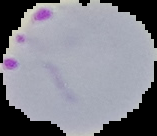

Image is 157×136 pixels. From a thin blood smear. Segmented cell region on a black background. Result: malaria parasites detected.